Assess this cell for malaria.
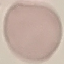

It is uninfected.

capture = smartphone camera at the microscope eyepiece
preparation = thin smear
image type = cell patch, automatically extracted from a larger field of view and resized to 64 × 64 pixels
stain = Giemsa